Classify this cell by malaria status.
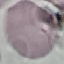
Uninfected.

Photographed with a smartphone camera at the microscope eyepiece. Automatically extracted cell patch, resized to 64 × 64 pixels. Thin blood film. Giemsa stain.